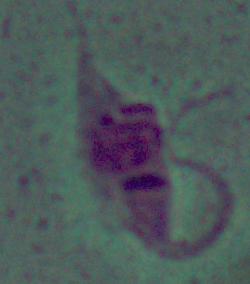 Micrograph. 1000x magnification. A Leishmania parasite is seen.